Outline each uninfected red blood cell.
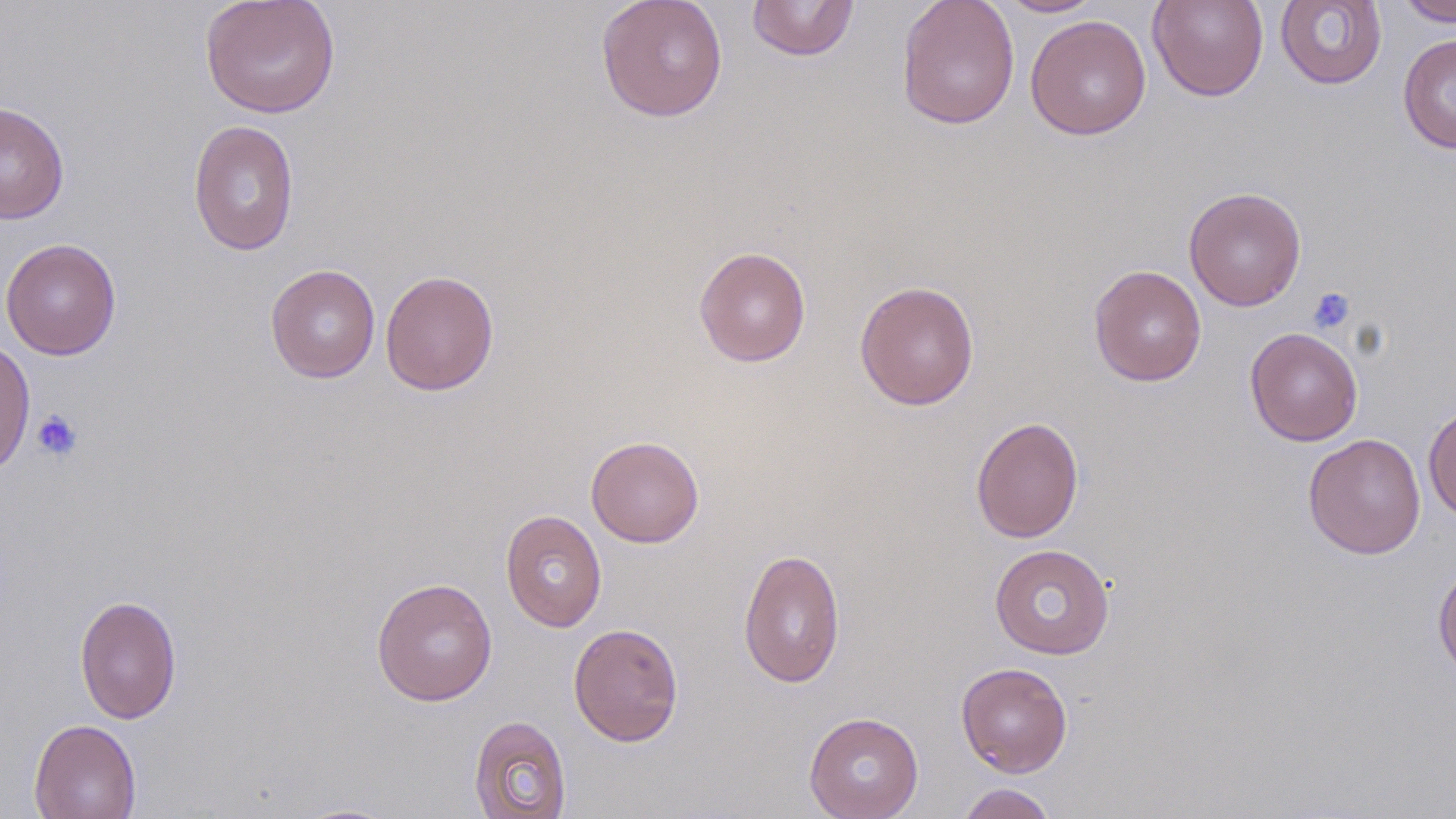
Approximate bounding boxes as (x1,y1)-(x2,y2) corner pairs in pixels.
Uninfected red blood cells: (200,0)-(340,118), (595,0)-(729,122), (896,0)-(1020,130), (993,0)-(1106,17), (1147,0)-(1269,102), (1396,0)-(1456,27), (746,1)-(860,61), (1275,1)-(1388,90), (1025,15)-(1151,140), (1397,33)-(1456,154), (0,101)-(70,225), (187,120)-(299,256), (1184,186)-(1306,311), (1,238)-(122,360), (694,246)-(812,367), (265,264)-(380,383), (1088,264)-(1207,387), (380,269)-(500,396), (854,280)-(980,410), (1245,327)-(1363,446), (0,337)-(35,478), (1423,403)-(1456,521), (970,415)-(1084,543), (1303,433)-(1427,559), (586,435)-(704,548), (500,509)-(607,632), (989,543)-(1115,659), (738,547)-(845,688), (1432,558)-(1456,681), (371,577)-(497,706), (74,594)-(182,724), (568,622)-(684,746), (956,662)-(1073,778), (803,711)-(924,819), (469,715)-(571,819), (28,718)-(141,819), (956,783)-(1057,819).

Summary:
  - Platelet locations: (1306,286)-(1355,335), (31,409)-(83,461)
  - Slide-level diagnosis: negative for blood parasites
  - Stain: May-Grünwald-Giemsa
  - Preparation: thin blood smear
  - Field of view: single
  - Modality: optical microscopy
  - Image size: 1456×819 pixels
  - Magnification: 1000x